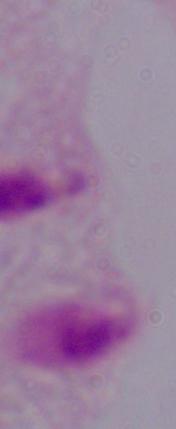
Summary:
  - Magnification: 1000x
  - Modality: photomicrograph
  - Identification: trichomonad